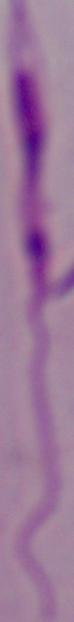 Micrograph. A Leishmania parasite is seen. Captured at 1000x magnification.